Name the blood parasite species.
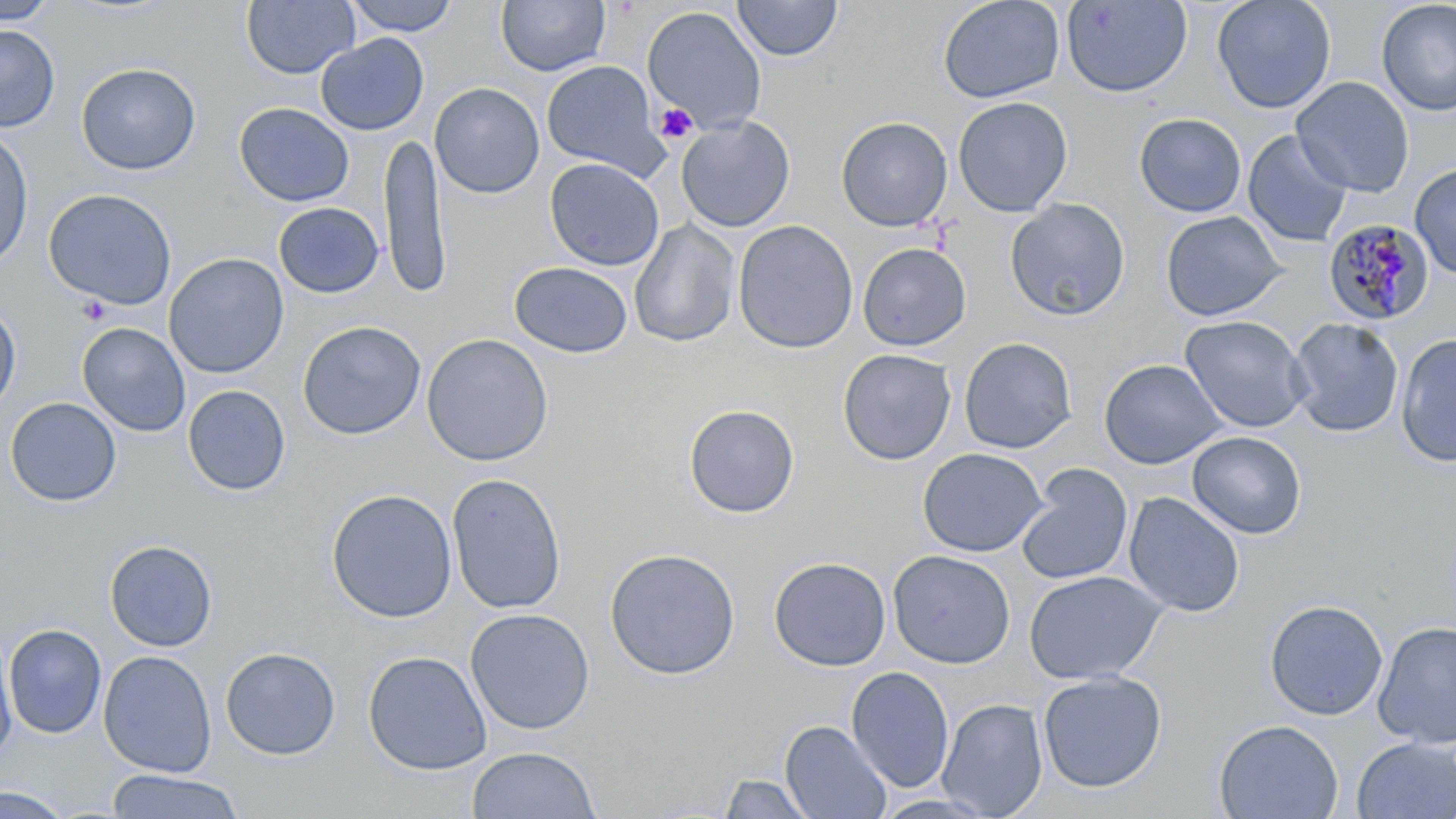
Plasmodium malariae.

Summary:
  - Coordinate format: approximate bounding boxes as (x1, y1, x2, y2) in pixels
  - Plasmodium malariae-infected red blood cell locations: (1322, 218, 1434, 327)
  - Uninfected red blood cell locations: (0, 0, 58, 24), (241, 0, 360, 79), (342, 0, 461, 36), (495, 0, 610, 76), (732, 0, 844, 62), (937, 0, 1066, 104), (1212, 0, 1336, 114), (1376, 0, 1456, 116), (1060, 1, 1193, 98), (642, 5, 767, 134), (0, 24, 59, 132), (316, 33, 429, 136), (540, 60, 668, 180), (76, 62, 201, 175), (1291, 77, 1414, 197), (430, 82, 545, 198), (952, 96, 1074, 217), (234, 102, 354, 207), (1134, 113, 1247, 217), (675, 115, 796, 232), (835, 116, 953, 232), (0, 125, 34, 269), (379, 129, 451, 300), (1242, 130, 1354, 248), (544, 157, 665, 271), (1410, 163, 1456, 280), (43, 188, 177, 310), (1005, 198, 1131, 321), (273, 202, 383, 298), (1160, 210, 1288, 322), (629, 219, 741, 348), (733, 220, 858, 353), (857, 242, 972, 351), (164, 253, 289, 378), (509, 261, 633, 358), (0, 299, 21, 415), (1179, 315, 1312, 433), (1288, 317, 1404, 437), (297, 320, 427, 440), (77, 322, 191, 437), (421, 333, 554, 467), (1395, 333, 1456, 468), (958, 337, 1078, 454), (837, 349, 956, 466), (1098, 358, 1228, 469), (182, 385, 291, 497), (5, 397, 121, 506), (682, 403, 801, 519), (1187, 431, 1307, 539), (917, 447, 1049, 558), (1016, 463, 1134, 586), (446, 473, 567, 614), (325, 488, 458, 623), (1123, 492, 1245, 617), (104, 540, 218, 652), (603, 547, 741, 680), (887, 550, 1015, 669), (768, 556, 891, 671), (1024, 570, 1168, 685), (1265, 599, 1388, 720), (464, 608, 595, 735), (1373, 620, 1456, 749), (2, 623, 108, 739), (0, 632, 18, 764), (220, 646, 341, 759), (98, 650, 217, 777), (362, 650, 492, 775), (846, 666, 955, 794), (1037, 671, 1167, 793), (937, 697, 1048, 818), (1214, 719, 1344, 818), (780, 720, 891, 819), (1351, 737, 1456, 819), (467, 746, 599, 819), (105, 769, 245, 819), (719, 773, 816, 818), (0, 785, 74, 819), (871, 793, 999, 818)
  - Platelet locations: (654, 102, 699, 145), (75, 295, 112, 326)
  - Stain: May-Grünwald-Giemsa
  - Field of view: one of a larger specimen
  - Magnification: 1000x
  - Preparation: thin blood film
  - Image size: 1456×819 pixels
  - Modality: light microscopy